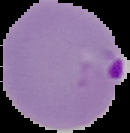

preparation = thin blood smear
image type = segmented cell region with the area outside set to black
result = Plasmodium parasites detected
image size = 130×133 pixels